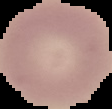

Malaria status: uninfected. Image is 112×109 pixels. Segmented cell region on a black background. From a thin blood film.